Name the cell type shown.
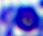

A leukocyte.

Captured at 400x magnification. Photomicrograph.